Comment on the morphology of the red blood cells.
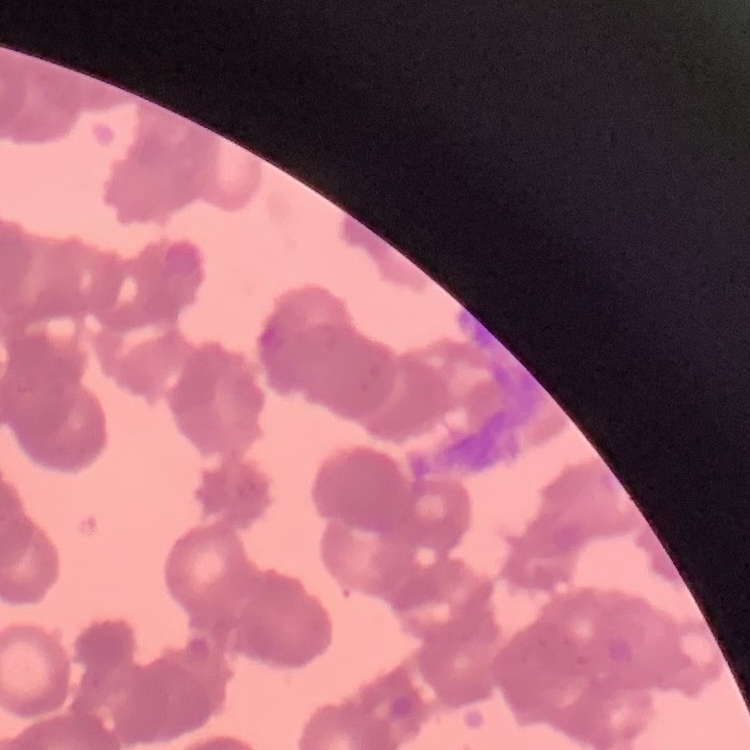
They show rouleaux formation.

Field's or Giemsa stain. One tile cut from a larger photomicrograph. Thin blood smear.